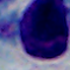

magnification = 1000x
identification = leukocyte
modality = photomicrograph